Comment on the morphology of the red blood cells.
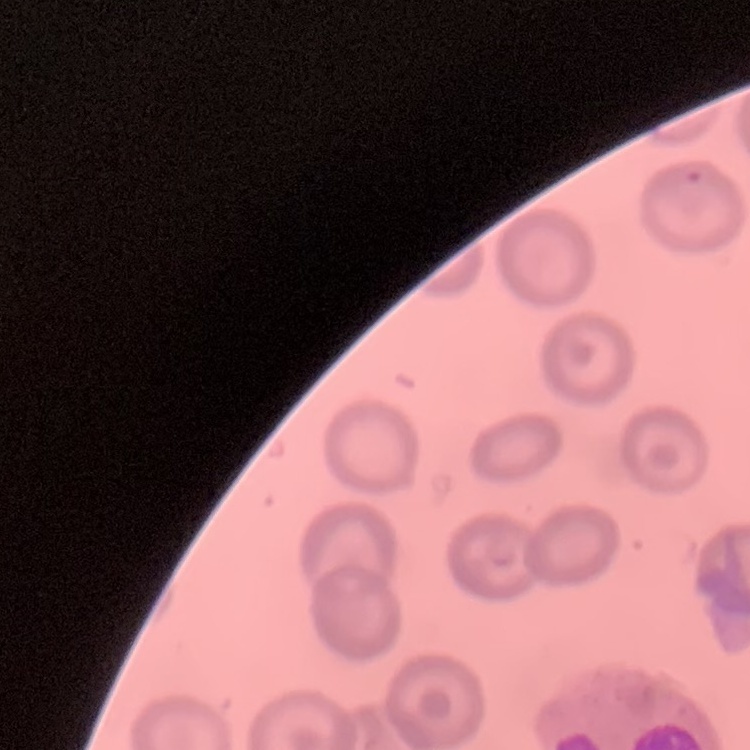

No rouleaux formation.

Summary:
  - Image type: square crop of a larger photomicrograph
  - Stain: Field's or Giemsa
  - Preparation: thin blood smear